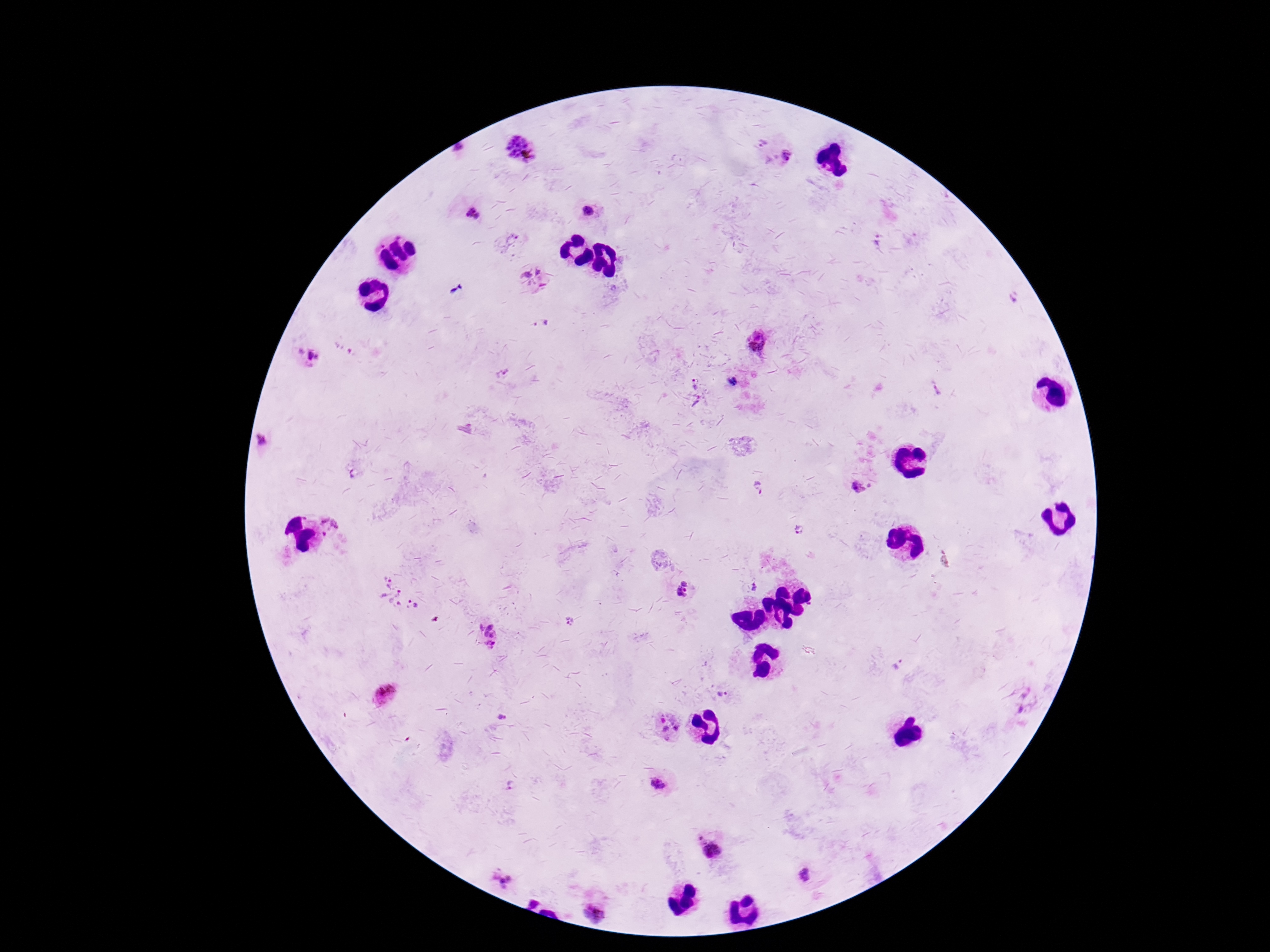

{
  "image_size": "1270×952 pixels",
  "preparation": "thick blood film",
  "capture": "smartphone camera through the microscope eyepiece",
  "plasmodium_parasite_locations": "approximate object centers, in pixels from the top-left corner: (x=763, y=144), (x=459, y=149), (x=523, y=150), (x=787, y=155), (x=588, y=212), (x=473, y=214), (x=515, y=235), (x=877, y=241), (x=538, y=272), (x=526, y=276), (x=457, y=289), (x=1012, y=298), (x=541, y=322), (x=756, y=341), (x=309, y=355), (x=318, y=357), (x=501, y=373), (x=732, y=382), (x=694, y=384), (x=936, y=391), (x=697, y=402), (x=261, y=439), (x=352, y=473), (x=870, y=486), (x=759, y=489), (x=857, y=489), (x=329, y=527), (x=799, y=530), (x=684, y=583), (x=754, y=587), (x=685, y=590), (x=681, y=591), (x=398, y=594), (x=569, y=621), (x=481, y=627), (x=489, y=627), (x=486, y=634), (x=492, y=635), (x=490, y=644), (x=896, y=664), (x=722, y=694), (x=385, y=695), (x=1026, y=695), (x=1021, y=710), (x=502, y=716), (x=663, y=721), (x=676, y=727), (x=665, y=729), (x=667, y=738), (x=657, y=783), (x=512, y=785), (x=700, y=838), (x=712, y=851), (x=805, y=876), (x=507, y=883), (x=534, y=903), (x=595, y=915)",
  "field_of_view": "one from this slide",
  "magnification": "100x",
  "patient_malaria_status": "infected",
  "stain": "Giemsa"
}